Identify the blood parasite species.
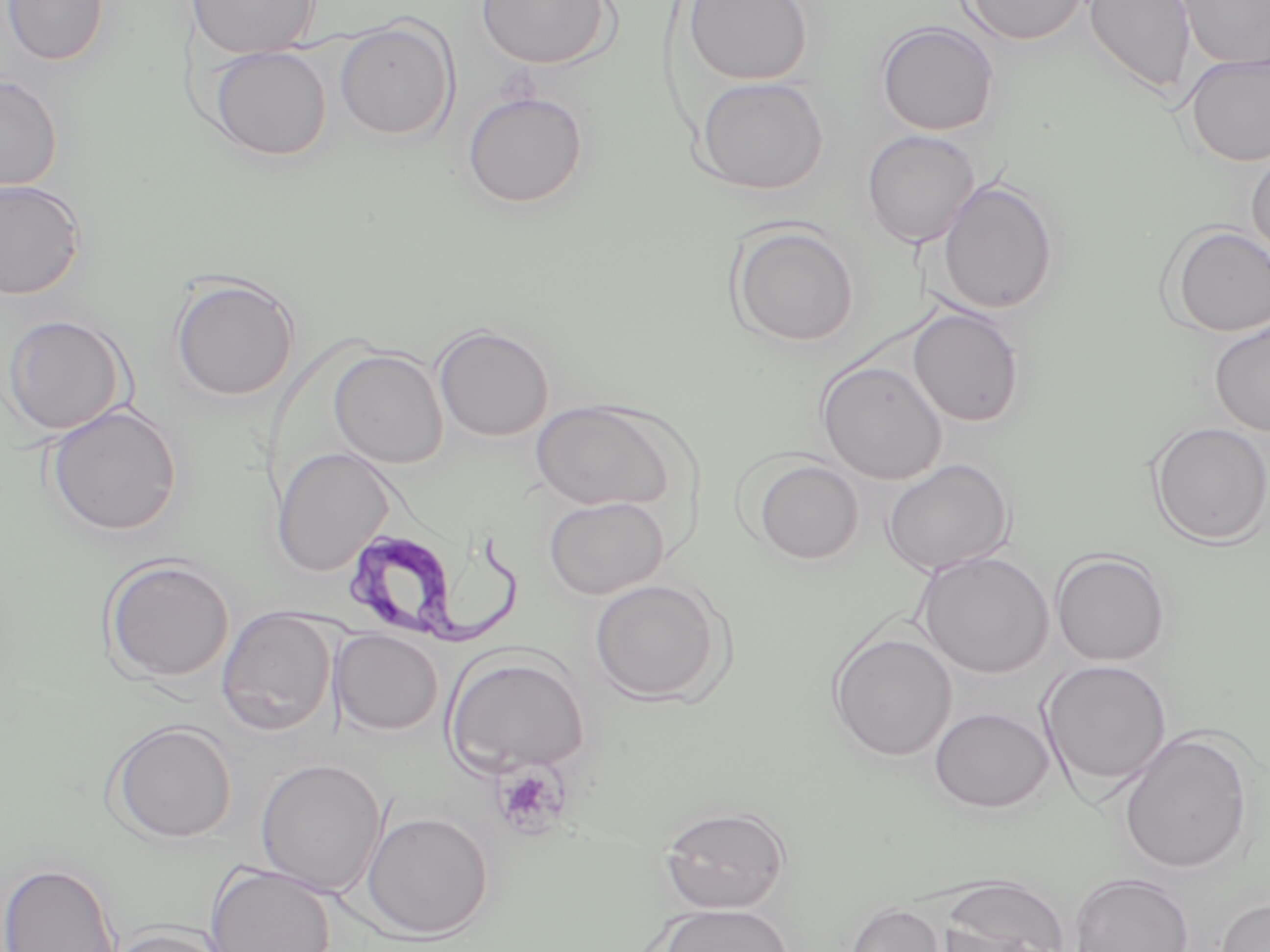
Trypanosoma brucei.

Summary:
  - Coordinate format: approximate bounding boxes as (x1, y1, x2, y2) in pixels
  - Trypanosoma brucei locations: (352, 523, 524, 648)
  - Platelet locations: (490, 761, 570, 841)
  - Uninfected red blood cell locations: (2, 0, 109, 65), (186, 0, 321, 58), (683, 0, 813, 85), (959, 0, 1091, 46), (1084, 0, 1195, 95), (476, 1, 613, 70), (1176, 1, 1270, 71), (334, 19, 458, 141), (876, 21, 1000, 136), (209, 46, 332, 161), (1182, 52, 1270, 167), (0, 73, 63, 191), (693, 76, 829, 195), (462, 90, 589, 210), (861, 130, 980, 248), (1246, 149, 1270, 265), (936, 178, 1060, 315), (0, 179, 86, 299), (727, 222, 860, 348), (1164, 224, 1270, 338), (169, 272, 300, 402), (907, 307, 1026, 427), (1, 315, 129, 436), (1208, 317, 1270, 436), (433, 324, 555, 442), (328, 349, 448, 468), (816, 359, 947, 483), (530, 400, 678, 511), (44, 404, 183, 537), (1147, 422, 1270, 547), (271, 446, 396, 578), (750, 458, 865, 565), (881, 458, 1015, 577), (543, 495, 669, 599), (1050, 550, 1172, 667), (916, 551, 1055, 678), (101, 556, 235, 684), (588, 578, 729, 704), (216, 606, 338, 736), (331, 629, 443, 735), (827, 631, 958, 762), (443, 652, 590, 778), (1038, 659, 1173, 790), (928, 706, 1055, 813), (107, 720, 238, 844), (1118, 730, 1254, 873), (256, 757, 387, 898), (658, 804, 791, 914), (361, 810, 494, 940), (0, 861, 122, 952), (204, 864, 336, 952), (1069, 872, 1195, 952), (935, 875, 1073, 952), (1216, 897, 1270, 952), (654, 903, 794, 952), (843, 903, 947, 952), (102, 925, 233, 952)
  - Stain: May-Grünwald-Giemsa
  - Magnification: 1000x
  - Image size: 1270×952 pixels
  - Preparation: thin blood smear
  - Field of view: single
  - Modality: optical microscopy